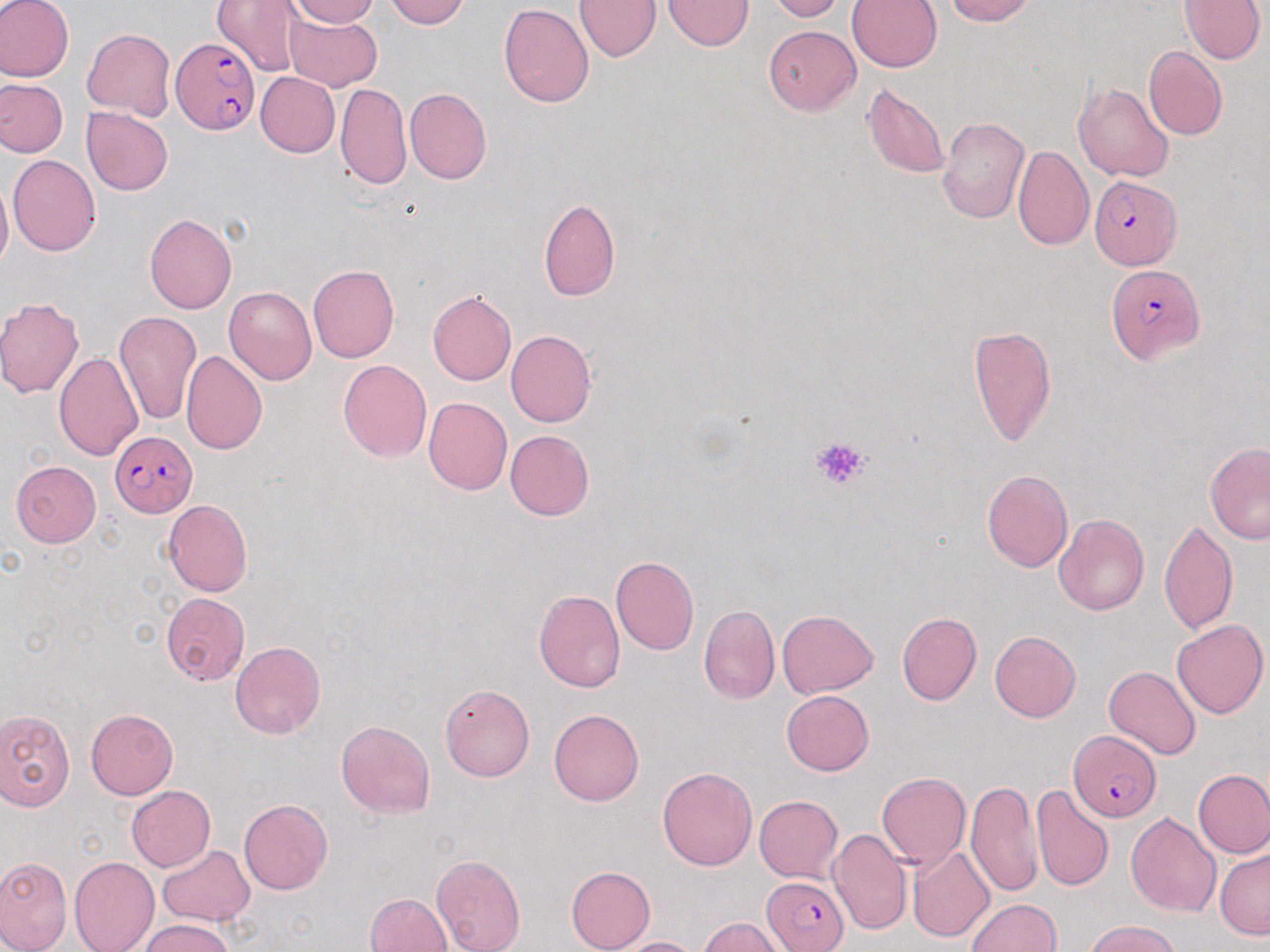
Approximate bounding boxes as (x1, y1, x2, y2) in pixels. Plasmodium falciparum-infected red blood cell locations: (171, 36, 259, 136), (1091, 176, 1181, 269), (1108, 265, 1204, 363), (110, 431, 197, 516), (1067, 729, 1161, 823), (763, 876, 852, 952). Uninfected red blood cell locations: (1, 0, 75, 83), (215, 0, 306, 76), (288, 0, 379, 27), (384, 0, 468, 28), (575, 0, 663, 62), (664, 0, 754, 50), (768, 0, 843, 21), (945, 0, 1033, 25), (1180, 0, 1266, 64), (848, 1, 942, 72), (498, 3, 594, 107), (283, 12, 382, 92), (764, 25, 860, 116), (82, 28, 176, 120), (1144, 47, 1226, 140), (255, 72, 339, 157), (0, 79, 68, 157), (1073, 81, 1174, 182), (335, 82, 411, 190), (863, 83, 949, 179), (404, 88, 492, 184), (81, 108, 173, 196), (935, 115, 1029, 223), (1013, 145, 1094, 249), (8, 154, 100, 256), (0, 177, 12, 273), (539, 197, 620, 301), (144, 213, 237, 313), (308, 265, 399, 363), (224, 286, 317, 385), (427, 291, 516, 385), (0, 298, 85, 398), (113, 310, 202, 427), (967, 325, 1055, 446), (505, 330, 596, 427), (182, 349, 268, 454), (54, 350, 145, 462), (338, 360, 432, 461), (423, 397, 512, 497), (504, 430, 595, 519), (1204, 442, 1270, 544), (10, 461, 101, 546), (982, 470, 1072, 572), (162, 500, 253, 597), (1054, 514, 1149, 615), (1160, 519, 1237, 635), (610, 556, 699, 656), (534, 590, 625, 692), (159, 592, 251, 685), (698, 606, 779, 703), (777, 609, 879, 699), (897, 612, 982, 705), (1172, 619, 1268, 719), (989, 631, 1081, 722), (231, 641, 326, 738), (1104, 665, 1200, 759), (439, 683, 534, 781), (781, 690, 874, 776), (0, 707, 75, 810), (86, 709, 177, 800), (549, 709, 644, 807), (336, 720, 435, 819), (658, 767, 756, 870), (1193, 770, 1270, 858), (877, 772, 971, 871), (966, 779, 1042, 898), (1031, 784, 1113, 890), (126, 786, 215, 872), (754, 794, 843, 882), (239, 799, 333, 895), (1126, 812, 1220, 917), (827, 826, 912, 936), (157, 844, 254, 926), (907, 845, 995, 942), (1215, 848, 1270, 940), (432, 854, 525, 952), (0, 855, 72, 952), (69, 856, 159, 952), (566, 865, 654, 952), (365, 892, 453, 952), (965, 898, 1059, 951), (698, 917, 790, 952), (137, 918, 236, 951), (1085, 919, 1182, 952), (613, 936, 703, 952). Platelet locations: (810, 435, 870, 491). Slide-level diagnosis: Plasmodium falciparum. Image is 1270×952 pixels. Single field of view. 1000x magnification. May-Grünwald-Giemsa stain. Thin blood film. Light microscopy.